Outline every leukocyte.
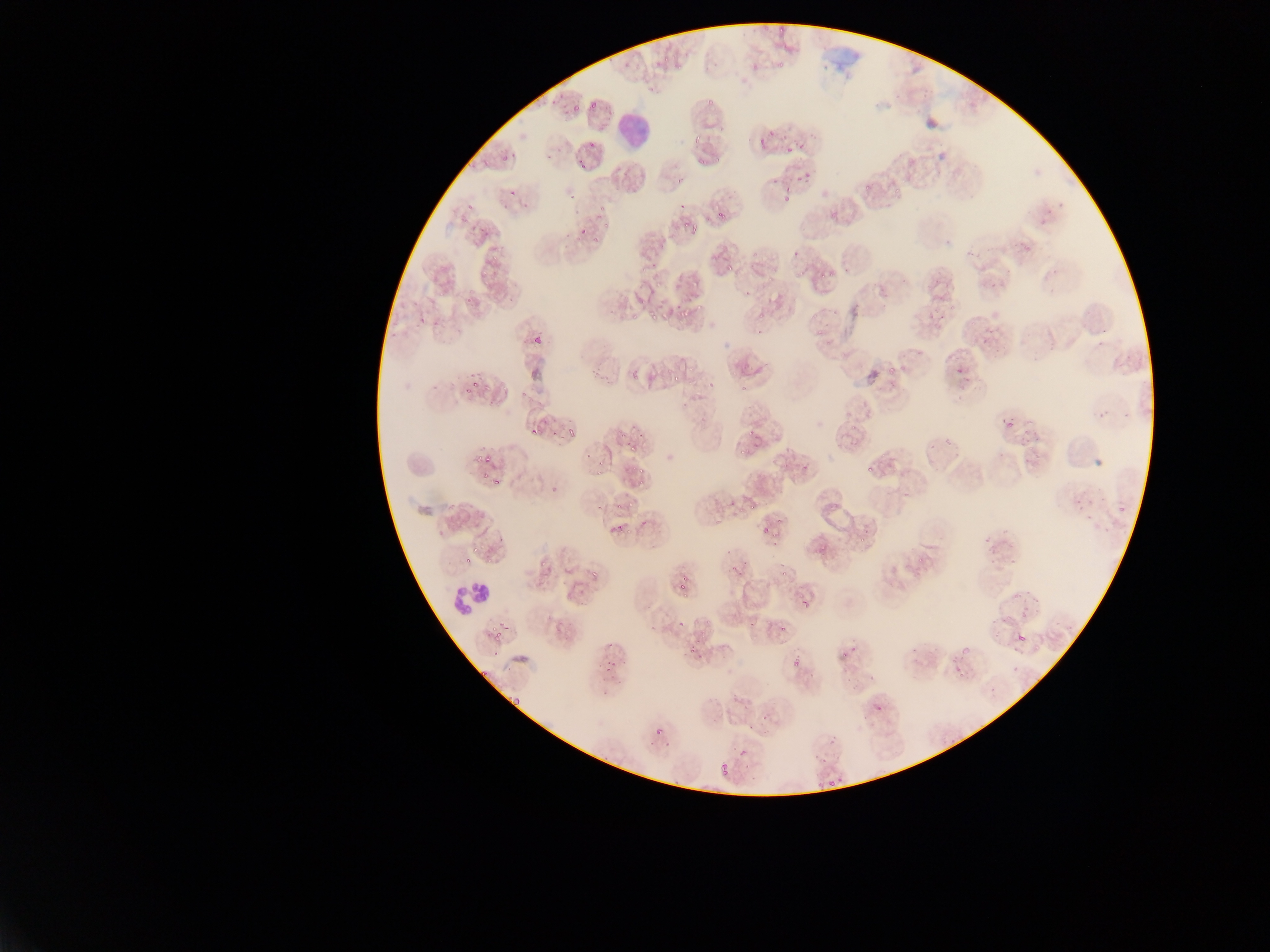

Approximate bounding boxes as {left, top, right, bottom} in pixels.
Leukocytes: {614, 112, 650, 153}, {452, 577, 486, 621}.

Malaria parasite locations: {762, 23, 775, 33}, {776, 23, 788, 33}, {776, 59, 786, 68}, {705, 91, 719, 107}, {571, 103, 581, 111}, {692, 133, 705, 147}, {758, 137, 769, 144}, {588, 141, 597, 149}, {758, 144, 765, 153}, {786, 146, 797, 154}, {714, 151, 725, 162}, {579, 159, 588, 170}, {804, 170, 811, 179}, {676, 175, 689, 185}, {862, 182, 872, 190}, {781, 191, 794, 202}, {598, 204, 605, 213}, {718, 207, 729, 217}, {596, 212, 602, 220}, {677, 215, 699, 229}, {605, 221, 611, 229}, {581, 229, 590, 233}, {790, 249, 804, 256}, {729, 265, 733, 273}, {637, 269, 648, 275}, {767, 277, 776, 282}, {463, 295, 472, 303}, {696, 297, 716, 313}, {682, 309, 690, 318}, {649, 312, 661, 323}, {417, 314, 434, 324}, {757, 315, 763, 323}, {934, 315, 944, 324}, {755, 326, 765, 335}, {816, 327, 827, 335}, {532, 338, 545, 346}, {824, 340, 829, 349}, {954, 368, 968, 380}, {629, 371, 639, 380}, {742, 386, 751, 390}, {466, 387, 474, 393}, {1005, 415, 1014, 429}, {563, 425, 579, 438}, {532, 427, 542, 435}, {623, 437, 640, 455}, {739, 447, 747, 455}, {475, 456, 483, 463}, {596, 456, 605, 477}, {485, 457, 494, 462}, {802, 459, 817, 473}, {867, 463, 874, 472}, {636, 464, 648, 472}, {482, 473, 491, 479}, {637, 475, 645, 488}, {550, 486, 558, 496}, {728, 491, 740, 508}, {1073, 492, 1096, 513}, {609, 497, 625, 516}, {1117, 502, 1133, 516}, {1085, 513, 1099, 534}, {776, 518, 785, 524}, {614, 524, 622, 532}, {761, 530, 770, 536}, {859, 533, 867, 541}, {471, 542, 480, 553}, {812, 543, 823, 556}, {540, 554, 554, 570}, {916, 554, 927, 563}, {466, 555, 475, 561}, {730, 562, 738, 573}, {780, 570, 789, 576}, {588, 571, 601, 580}, {680, 577, 690, 593}, {798, 595, 814, 612}, {1005, 610, 1013, 618}, {1021, 610, 1027, 620}, {691, 618, 699, 628}, {676, 620, 685, 630}, {779, 623, 789, 631}, {489, 625, 499, 631}, {708, 627, 714, 635}, {1012, 629, 1032, 649}, {496, 630, 502, 638}, {690, 647, 698, 656}, {959, 648, 967, 657}, {841, 651, 851, 658}, {790, 655, 804, 667}, {602, 656, 615, 671}, {480, 668, 490, 679}, {508, 696, 524, 715}, {873, 699, 890, 715}, {653, 726, 666, 739}, {736, 746, 750, 764}, {818, 751, 831, 765}, {717, 761, 734, 779}, {820, 775, 840, 790} | approximate {x, y} pixel centers of objects too small to bound: {594, 106}, {772, 133}, {703, 160}, {797, 179}, {897, 191}, {595, 240}, {801, 274}, {822, 275}, {823, 293}, {892, 371}, {676, 378}, {477, 385}, {750, 433}, {496, 482}, {750, 510}. Collected in Ghana. Mobile-phone photograph taken through the microscope. Thin blood film. Image is 1270×952 pixels. Single field of view.